Name the blood parasite species.
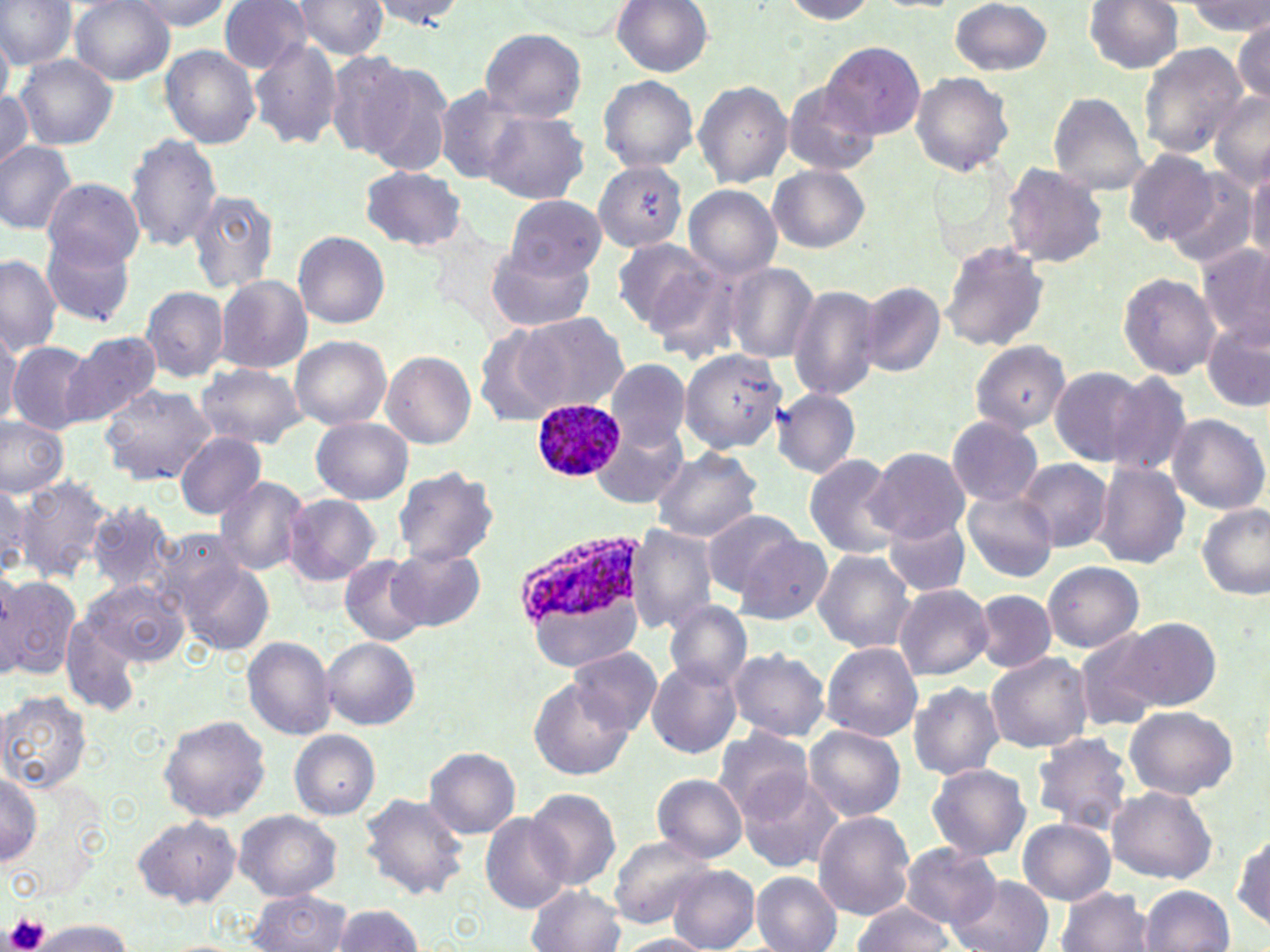

Plasmodium ovale.

Approximate bounding boxes as [x1, y1, x2, y2] in pixels. Plasmodium ovale-infected red blood cell locations: [530, 399, 625, 481], [511, 524, 643, 630]. Uninfected red blood cell locations: [0, 0, 75, 69], [70, 0, 175, 84], [127, 0, 231, 31], [217, 0, 313, 73], [371, 0, 467, 30], [291, 1, 389, 60], [611, 1, 713, 77], [778, 1, 878, 23], [949, 1, 1052, 76], [1084, 1, 1183, 74], [1183, 1, 1268, 35], [1232, 17, 1269, 103], [480, 27, 588, 121], [0, 31, 13, 110], [250, 38, 344, 150], [822, 42, 924, 140], [1138, 44, 1248, 157], [161, 46, 262, 148], [322, 50, 421, 158], [13, 54, 119, 151], [361, 61, 456, 178], [910, 70, 1015, 176], [598, 77, 698, 171], [781, 81, 880, 178], [693, 82, 791, 187], [432, 85, 530, 183], [0, 89, 32, 172], [1207, 91, 1270, 187], [1047, 94, 1149, 194], [482, 111, 588, 204], [125, 132, 222, 250], [0, 140, 76, 233], [1122, 149, 1218, 245], [1246, 161, 1270, 264], [594, 162, 688, 251], [1002, 162, 1111, 268], [767, 164, 869, 253], [360, 166, 467, 251], [1162, 167, 1261, 271], [44, 179, 143, 269], [684, 186, 781, 277], [187, 189, 280, 294], [504, 194, 605, 281], [294, 231, 388, 328], [611, 236, 718, 333], [40, 237, 137, 327], [939, 241, 1049, 353], [1198, 242, 1270, 347], [485, 247, 595, 334], [0, 254, 62, 356], [725, 263, 820, 362], [1119, 272, 1219, 378], [216, 275, 312, 374], [858, 283, 945, 376], [140, 285, 229, 382], [789, 285, 884, 401], [503, 312, 629, 415], [1203, 316, 1269, 413], [0, 326, 23, 421], [63, 332, 161, 428], [290, 336, 392, 429], [968, 340, 1072, 435], [8, 342, 97, 433], [679, 349, 784, 453], [380, 351, 476, 449], [605, 357, 691, 451], [193, 362, 305, 449], [1049, 367, 1149, 465], [1101, 371, 1196, 478], [97, 382, 217, 486], [770, 387, 860, 479], [1166, 413, 1268, 515], [946, 415, 1043, 507], [0, 416, 70, 496], [311, 417, 413, 503], [591, 417, 691, 510], [173, 434, 266, 519], [650, 446, 763, 542], [866, 447, 969, 542], [803, 454, 901, 557], [1017, 459, 1111, 552], [1090, 461, 1190, 569], [389, 466, 500, 569], [14, 475, 115, 582], [214, 476, 310, 576], [1, 482, 41, 573], [961, 489, 1058, 581], [282, 495, 381, 586], [88, 501, 177, 593], [1198, 503, 1269, 599], [700, 508, 804, 594], [884, 515, 972, 599], [627, 525, 718, 634], [151, 528, 248, 621], [736, 533, 834, 624], [389, 547, 485, 632], [811, 550, 916, 653], [339, 555, 430, 645], [179, 559, 275, 655], [1042, 562, 1144, 652], [0, 573, 80, 678], [83, 578, 187, 667], [893, 585, 994, 680], [974, 588, 1057, 674], [535, 594, 639, 668], [662, 600, 752, 690], [61, 615, 147, 717], [1108, 617, 1224, 715], [1075, 631, 1166, 730], [242, 637, 336, 740], [322, 638, 418, 729], [821, 642, 923, 741], [568, 647, 662, 735], [727, 649, 831, 741], [986, 652, 1093, 753], [645, 658, 742, 758], [527, 680, 633, 781], [905, 683, 1004, 779], [1, 690, 91, 792], [1123, 705, 1238, 801], [159, 716, 272, 822], [805, 726, 906, 820], [713, 728, 815, 821], [289, 730, 380, 820], [1032, 732, 1138, 833], [423, 747, 522, 840], [927, 763, 1031, 862], [0, 771, 42, 866], [652, 773, 748, 864], [737, 774, 841, 873], [1107, 785, 1218, 883], [525, 787, 624, 890], [357, 792, 470, 900], [234, 809, 343, 901], [813, 811, 916, 920], [480, 812, 572, 914], [132, 815, 242, 909], [1018, 818, 1115, 905], [1232, 825, 1268, 934], [607, 832, 715, 929], [898, 844, 1001, 929], [667, 866, 760, 951], [751, 870, 842, 952], [947, 875, 1051, 952], [527, 886, 626, 952], [1057, 886, 1155, 952], [1138, 886, 1235, 952], [247, 890, 354, 952], [333, 903, 421, 952], [849, 904, 957, 952], [33, 919, 130, 951], [616, 935, 713, 952]. Platelet locations: [3, 913, 50, 952]. Single field of view. Image is 1270×952 pixels. 1000x magnification. Thin blood film. Optical microscopy. May-Grünwald-Giemsa stain.